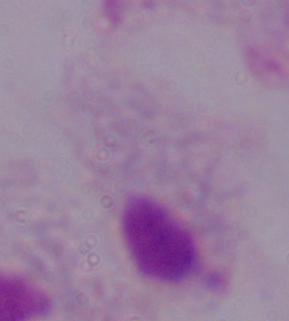
modality = micrograph
identification = trichomonad
magnification = 1000x